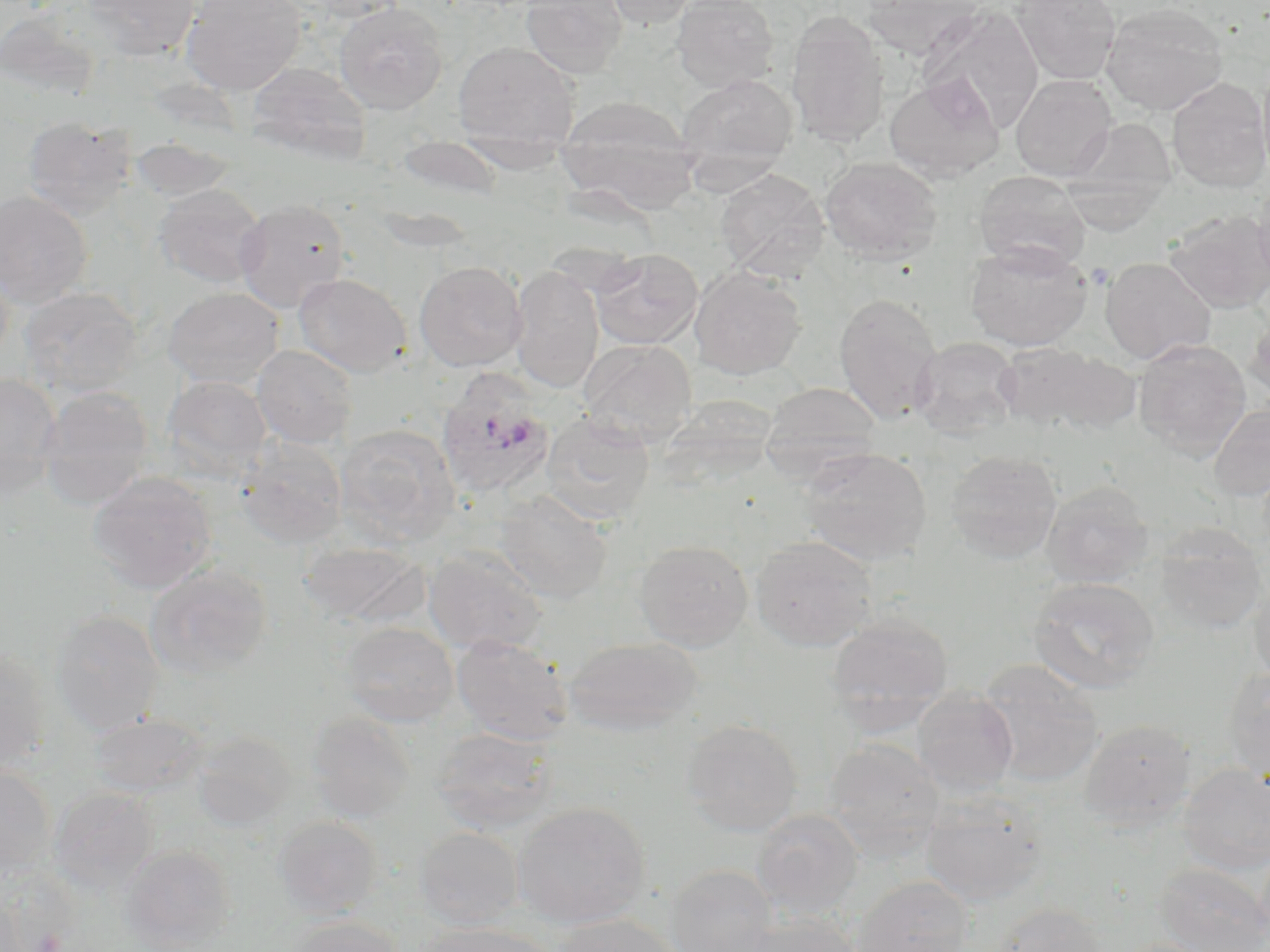
{
  "slide_level_diagnosis": "Plasmodium ovale",
  "uninfected_red_blood_cell_locations": "approximate bounding boxes as (x1, y1, x2, y2) in pixels: (83, 0, 201, 61), (180, 0, 307, 95), (521, 0, 629, 78), (600, 0, 702, 29), (671, 0, 780, 92), (863, 0, 981, 59), (1010, 0, 1121, 85), (333, 2, 449, 114), (1100, 2, 1229, 115), (919, 5, 1045, 135), (786, 11, 890, 149), (453, 42, 579, 147), (1257, 60, 1270, 185), (247, 62, 372, 164), (676, 73, 798, 182), (884, 73, 1005, 183), (1011, 75, 1117, 180), (1166, 77, 1270, 193), (555, 95, 701, 215), (1068, 99, 1263, 209), (21, 116, 136, 220), (1064, 119, 1177, 223), (395, 137, 502, 198), (129, 138, 236, 203), (820, 156, 942, 265), (716, 169, 829, 280), (974, 170, 1090, 272), (1060, 170, 1171, 235), (1253, 181, 1270, 290), (154, 184, 266, 288), (0, 190, 93, 308), (234, 199, 351, 313), (1164, 210, 1270, 313), (965, 240, 1092, 351), (591, 248, 703, 349), (1100, 256, 1216, 365), (0, 260, 14, 369), (414, 261, 528, 371), (508, 265, 605, 393), (689, 266, 807, 380), (294, 273, 412, 377), (18, 286, 143, 397), (162, 287, 284, 388), (833, 292, 943, 425), (1245, 313, 1270, 403), (910, 337, 1023, 438), (579, 339, 696, 448), (1133, 339, 1252, 460), (991, 341, 1115, 433), (252, 345, 358, 448), (1043, 351, 1144, 434), (0, 373, 62, 498), (161, 375, 272, 479), (760, 382, 882, 482), (38, 386, 154, 509), (1208, 403, 1270, 502), (541, 412, 655, 526), (336, 423, 460, 546), (235, 438, 348, 548), (798, 447, 932, 566), (944, 450, 1062, 563), (88, 472, 217, 593), (1041, 481, 1155, 588), (493, 491, 613, 604), (1154, 523, 1268, 636), (750, 534, 877, 652), (633, 539, 753, 652), (296, 541, 428, 628), (423, 548, 548, 655), (145, 563, 272, 680), (1248, 569, 1270, 687), (1028, 577, 1160, 694), (50, 610, 164, 734), (826, 614, 954, 725), (339, 621, 459, 726), (451, 634, 573, 745), (563, 636, 703, 735), (0, 647, 52, 773), (976, 659, 1105, 787), (1223, 667, 1270, 781), (911, 690, 1019, 797), (306, 711, 416, 821), (89, 713, 207, 798), (681, 718, 803, 836), (1079, 718, 1196, 829), (432, 727, 557, 834), (191, 730, 296, 829), (823, 737, 947, 858), (1177, 763, 1270, 875), (0, 766, 56, 879), (49, 787, 159, 893), (919, 791, 1048, 906), (512, 801, 651, 929), (751, 809, 865, 919), (272, 815, 382, 919), (415, 826, 524, 929), (121, 844, 236, 950), (1154, 862, 1270, 952), (664, 864, 779, 952), (0, 867, 77, 951), (851, 875, 974, 951), (0, 896, 32, 952), (992, 903, 1109, 952), (734, 913, 863, 952), (552, 914, 684, 952), (287, 916, 406, 952), (417, 921, 558, 952), (1112, 938, 1220, 952)",
  "modality": "light microscopy",
  "plasmodium_ovale_infected_red_blood_cell_locations": "approximate bounding boxes as (x1, y1, x2, y2) in pixels: (436, 370, 557, 501)",
  "field_of_view": "one of a larger specimen",
  "preparation": "thin blood smear",
  "magnification": "1000x",
  "stain": "May-Grünwald-Giemsa",
  "image_size": "1270×952 pixels"
}